Identify the parasite.
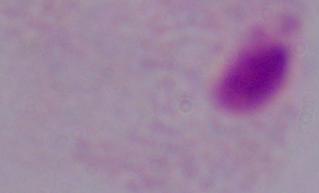
A trichomonad.

modality = photomicrograph
magnification = 1000x